Assess this cell for malaria.
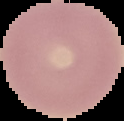

Uninfected.

Summary:
  - Image size: 124×121 pixels
  - Preparation: thin blood smear
  - Image type: segmented cell region with the area outside set to black